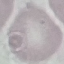 Result: no malaria parasites seen. Photographed with a smartphone camera at the microscope eyepiece. Cell patch, automatically extracted from a larger field of view and resized to 64 × 64 pixels. Thin smear of blood. Giemsa-stained preparation.